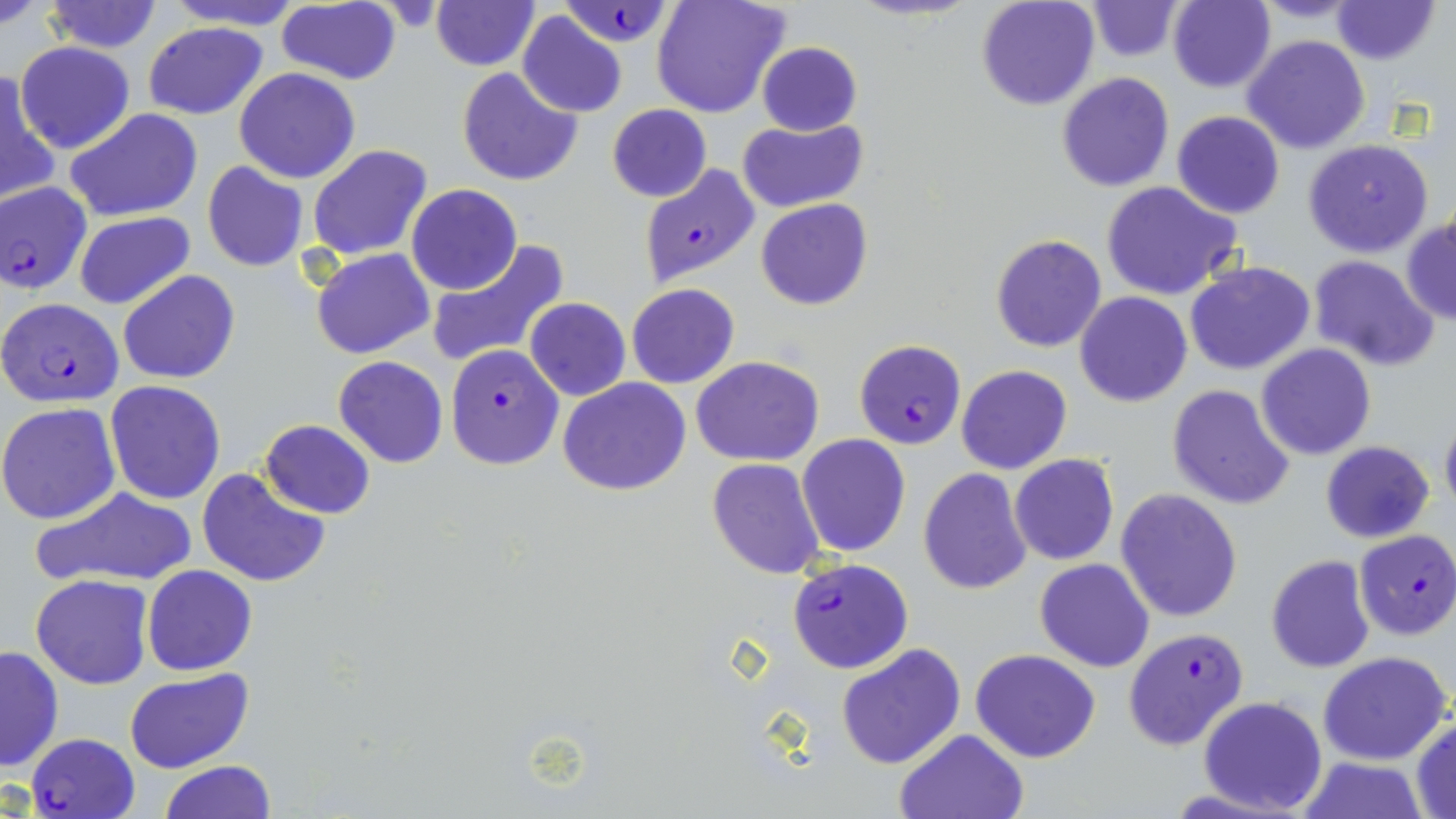
Summary:
  - Coordinate format: approximate bounding boxes as [x1, y1, x2, y2] in pixels
  - Plasmodium falciparum-infected red blood cell locations: [559, 0, 673, 50], [638, 164, 760, 287], [0, 182, 94, 296], [0, 297, 125, 408], [853, 339, 967, 449], [444, 345, 564, 470], [1354, 531, 1456, 640], [786, 557, 913, 674], [1124, 626, 1250, 752], [25, 732, 142, 819]
  - Uninfected red blood cell locations: [0, 0, 55, 29], [164, 0, 308, 29], [652, 0, 789, 119], [977, 0, 1101, 111], [1085, 0, 1185, 60], [1333, 0, 1438, 65], [42, 1, 163, 53], [1166, 1, 1276, 91], [275, 2, 401, 85], [431, 2, 539, 70], [517, 11, 627, 118], [143, 21, 268, 120], [1241, 36, 1369, 155], [15, 41, 135, 154], [757, 41, 862, 135], [456, 66, 583, 187], [234, 68, 361, 183], [1, 69, 60, 205], [1057, 72, 1174, 192], [607, 104, 712, 203], [66, 108, 203, 221], [1171, 110, 1285, 219], [739, 117, 870, 214], [1304, 139, 1433, 258], [307, 145, 433, 262], [203, 162, 309, 272], [1100, 180, 1242, 302], [406, 184, 522, 295], [756, 198, 872, 311], [1401, 211, 1456, 325], [74, 213, 194, 310], [989, 234, 1107, 352], [426, 241, 570, 369], [312, 249, 435, 360], [1307, 255, 1438, 370], [1185, 262, 1315, 377], [118, 269, 239, 384], [627, 283, 739, 388], [1075, 292, 1192, 407], [524, 298, 631, 402], [1256, 343, 1376, 460], [334, 356, 449, 469], [691, 356, 823, 466], [956, 365, 1072, 475], [558, 377, 692, 496], [104, 380, 226, 504], [1167, 384, 1296, 512], [0, 402, 121, 526], [1439, 408, 1456, 521], [260, 419, 376, 519], [796, 434, 911, 558], [1321, 441, 1434, 543], [1009, 454, 1119, 566], [706, 458, 826, 580], [195, 467, 330, 589], [918, 469, 1033, 594], [36, 486, 198, 589], [1115, 487, 1244, 623], [1265, 555, 1374, 673], [1036, 558, 1154, 672], [142, 565, 258, 676], [32, 574, 153, 689], [835, 642, 966, 770], [1, 645, 63, 773], [972, 647, 1101, 763], [1319, 651, 1452, 765], [124, 668, 254, 774], [1198, 696, 1327, 816], [1412, 716, 1456, 816], [895, 729, 1028, 818], [1299, 756, 1428, 818], [160, 761, 276, 818]
  - Slide-level diagnosis: Plasmodium falciparum
  - Field of view: single
  - Modality: light microscopy
  - Magnification: 1000x
  - Preparation: thin blood smear
  - Stain: May-Grünwald-Giemsa
  - Image size: 1456×819 pixels